Classify this cell by malaria status.
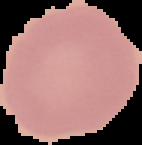

It is uninfected.

preparation = thin blood film
image type = segmented cell region with the area outside set to black
image size = 142×145 pixels